Assess this cell for malaria.
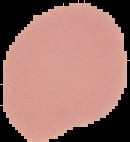
Uninfected.

preparation = thin blood smear
image type = segmented cell region on a black background
image size = 130×142 pixels